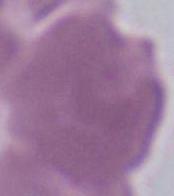
Captured at 1000x magnification. Micrograph. An erythrocyte is seen.